Classify this cell by malaria status.
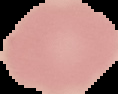

It is uninfected.

Cell region segmented out of the field of view; the surrounding area is masked to black. From a thin blood film. Image is 118×94 pixels.